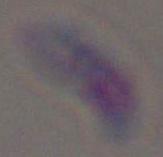

Toxoplasma gondii is shown. Micrograph. 1000x magnification.